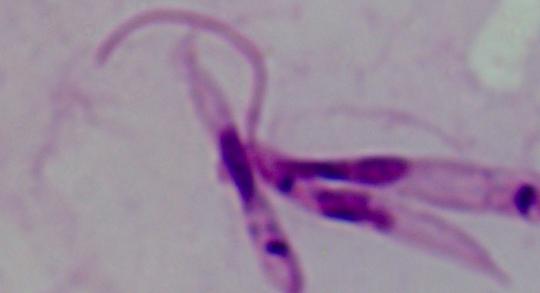
Summary:
  - Magnification: 1000x
  - Identification: Leishmania
  - Modality: micrograph